Assess the morphology of the erythrocytes.
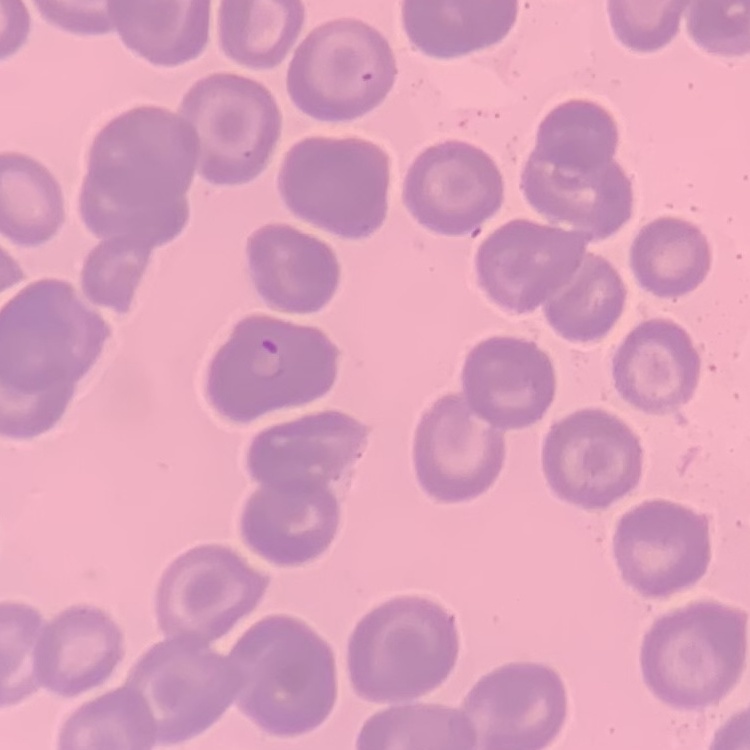

No rouleaux formation.

Field's or Giemsa stain. One tile cut from a larger photomicrograph. Thin peripheral smear.